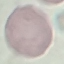

Summary:
  - Malaria status: uninfected
  - Capture: smartphone through the microscope eyepiece
  - Stain: Giemsa
  - Preparation: thin smear
  - Image type: automatically extracted cell patch, resized to 64 × 64 pixels